State the preparation type.
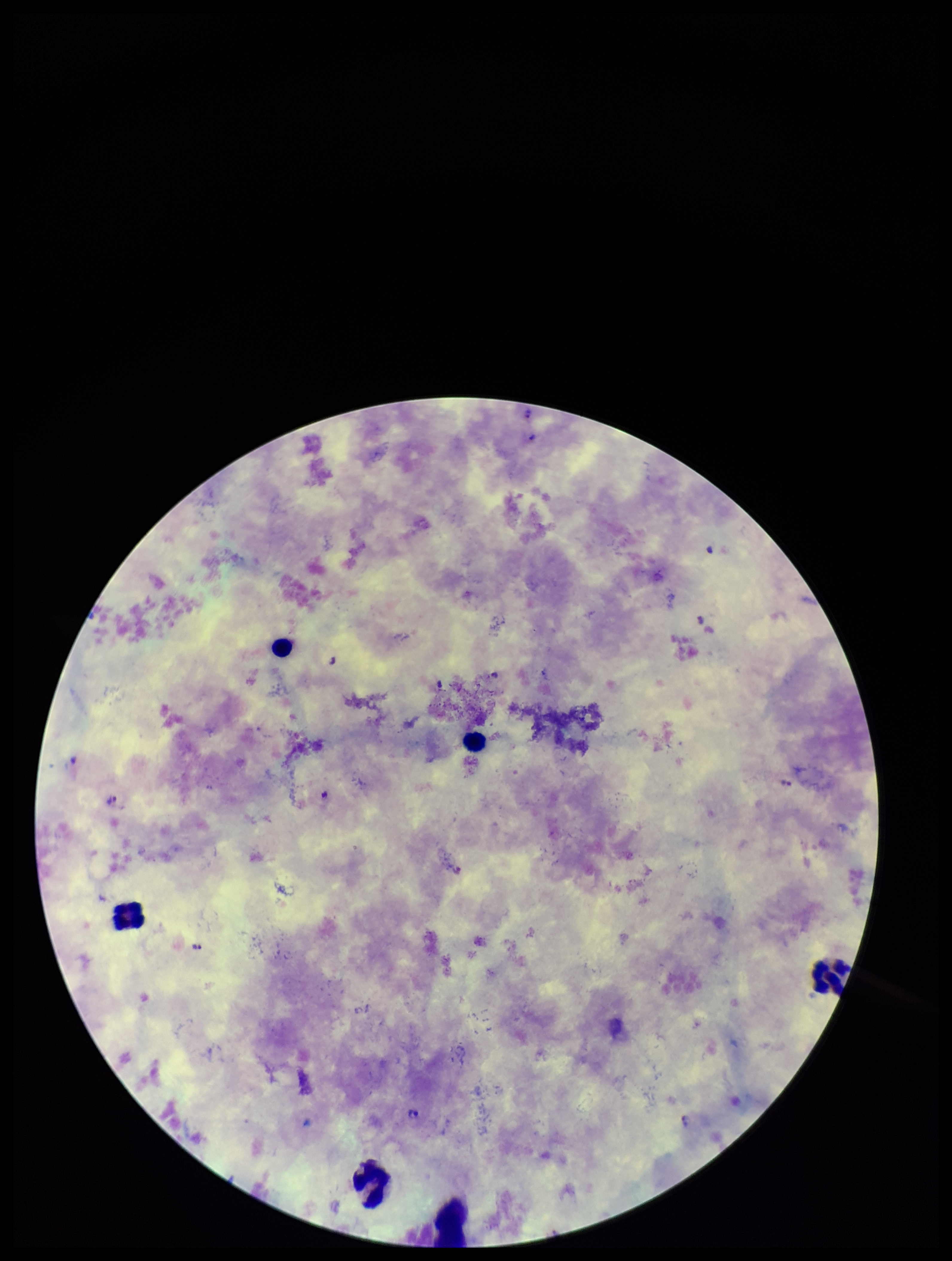
A thick smear.

field of view = single
species reported for this patient = Plasmodium falciparum
Plasmodium parasites = identified
leukocyte count = 6
stain = Giemsa
patient malaria status = positive
image size = 952×1261 pixels
capture = smartphone photograph through the microscope eyepiece
parasite count = 10